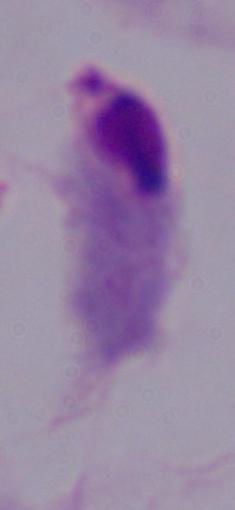

Summary:
  - Magnification: 1000x
  - Modality: photomicrograph
  - Identification: trichomonad